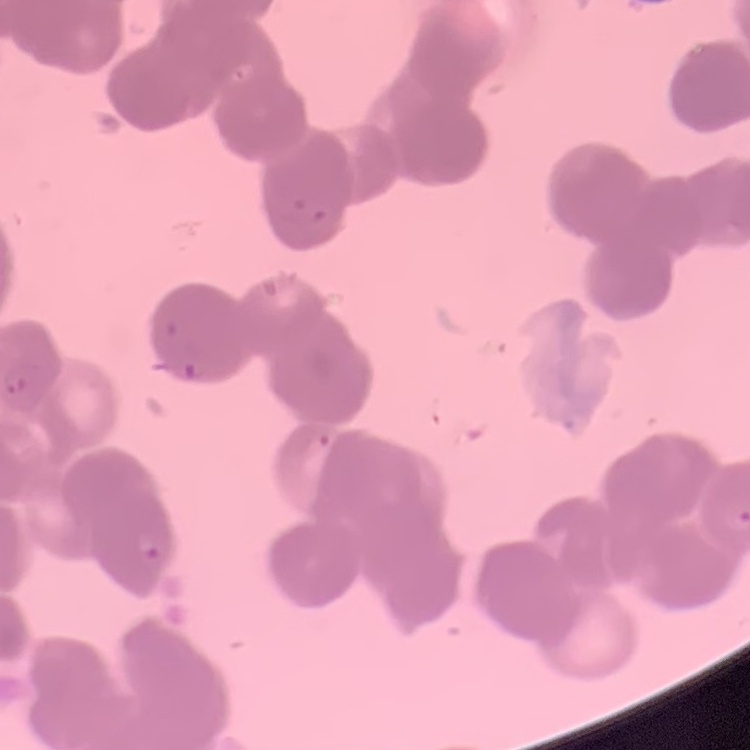 The red blood cells show rouleaux formation. Field's or Giemsa stain. Thin blood smear. One tile cut from a larger photomicrograph.